Identify the parasite.
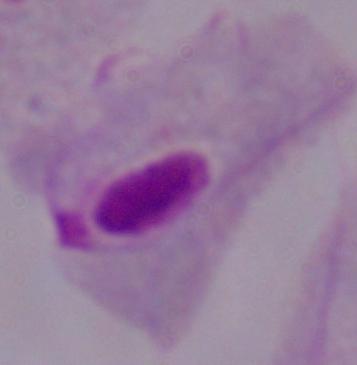

A trichomonad.

modality: micrograph
magnification: 1000x